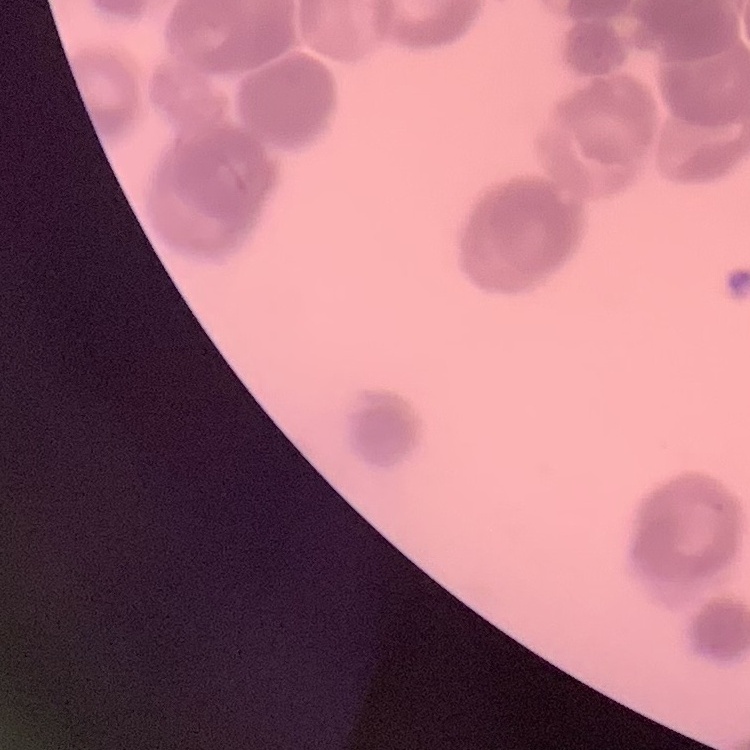
Summary:
  - Red blood cell morphology: rouleaux formation
  - Preparation: thin blood film
  - Stain: Field's or Giemsa
  - Image type: one tile cut from a larger photomicrograph